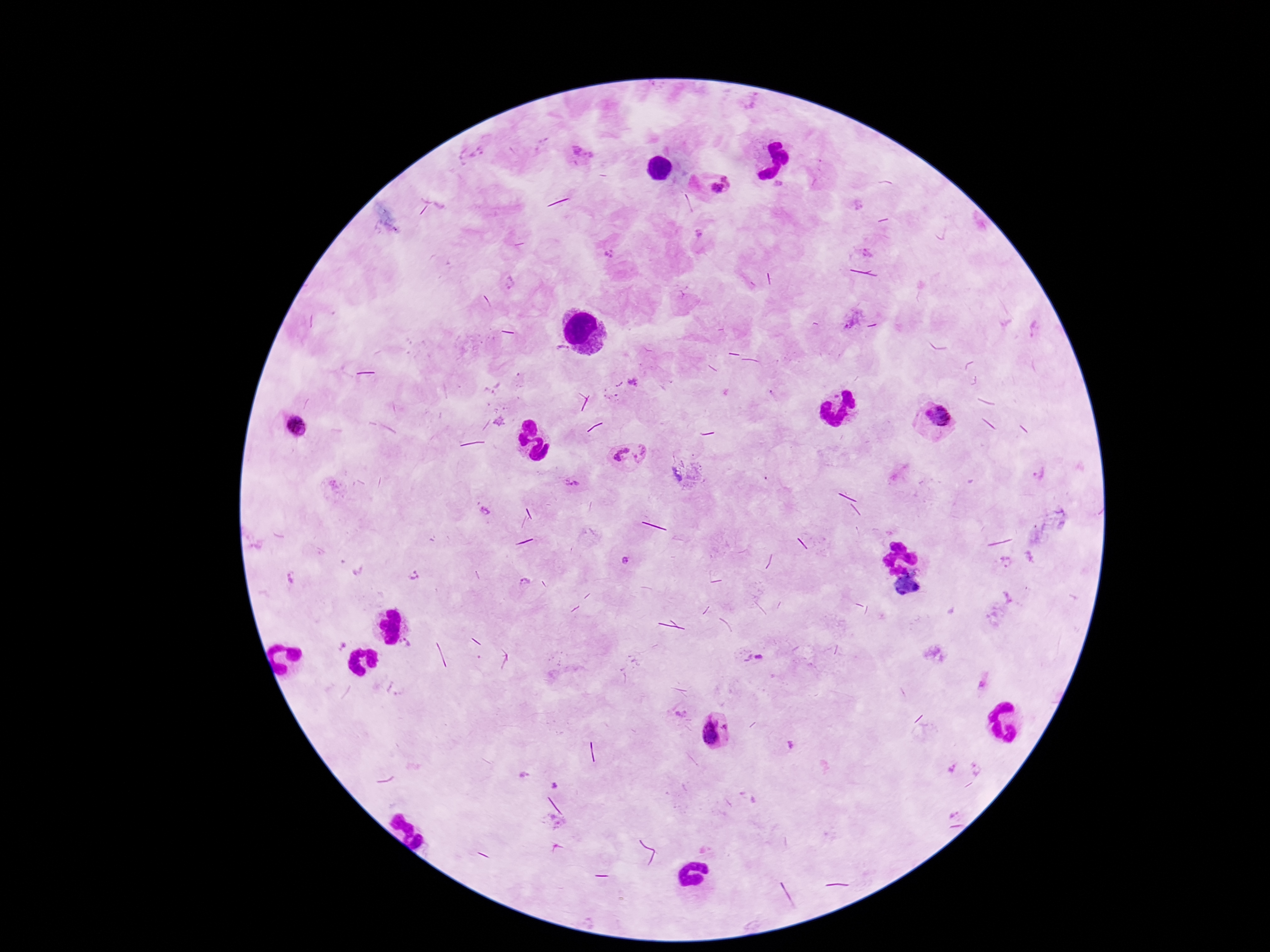

Approximate centers as [x, y] in pixels.
Summary:
  - Plasmodium parasite locations: [576, 150], [592, 155], [728, 178], [716, 188], [699, 233], [610, 254], [510, 283], [851, 319], [1034, 329], [563, 353], [633, 383], [934, 416], [296, 426], [620, 452], [644, 454], [1039, 473], [572, 483], [488, 510], [626, 561], [1006, 562], [292, 575], [415, 576], [524, 581], [406, 643], [758, 657], [983, 684], [396, 690], [680, 714], [715, 730], [790, 745], [976, 768], [950, 770], [525, 774], [556, 785], [957, 813]
  - Capture: smartphone camera through the microscope eyepiece
  - Stain: Giemsa
  - Image size: 1270×952 pixels
  - Patient malaria status: positive
  - Field of view: one from this slide
  - Preparation: thick peripheral-blood smear
  - Magnification: 100x